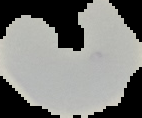 The area outside the segmented cell region is set to black. Image is 142×118 pixels. Result: Plasmodium parasites detected. From a thin blood film.